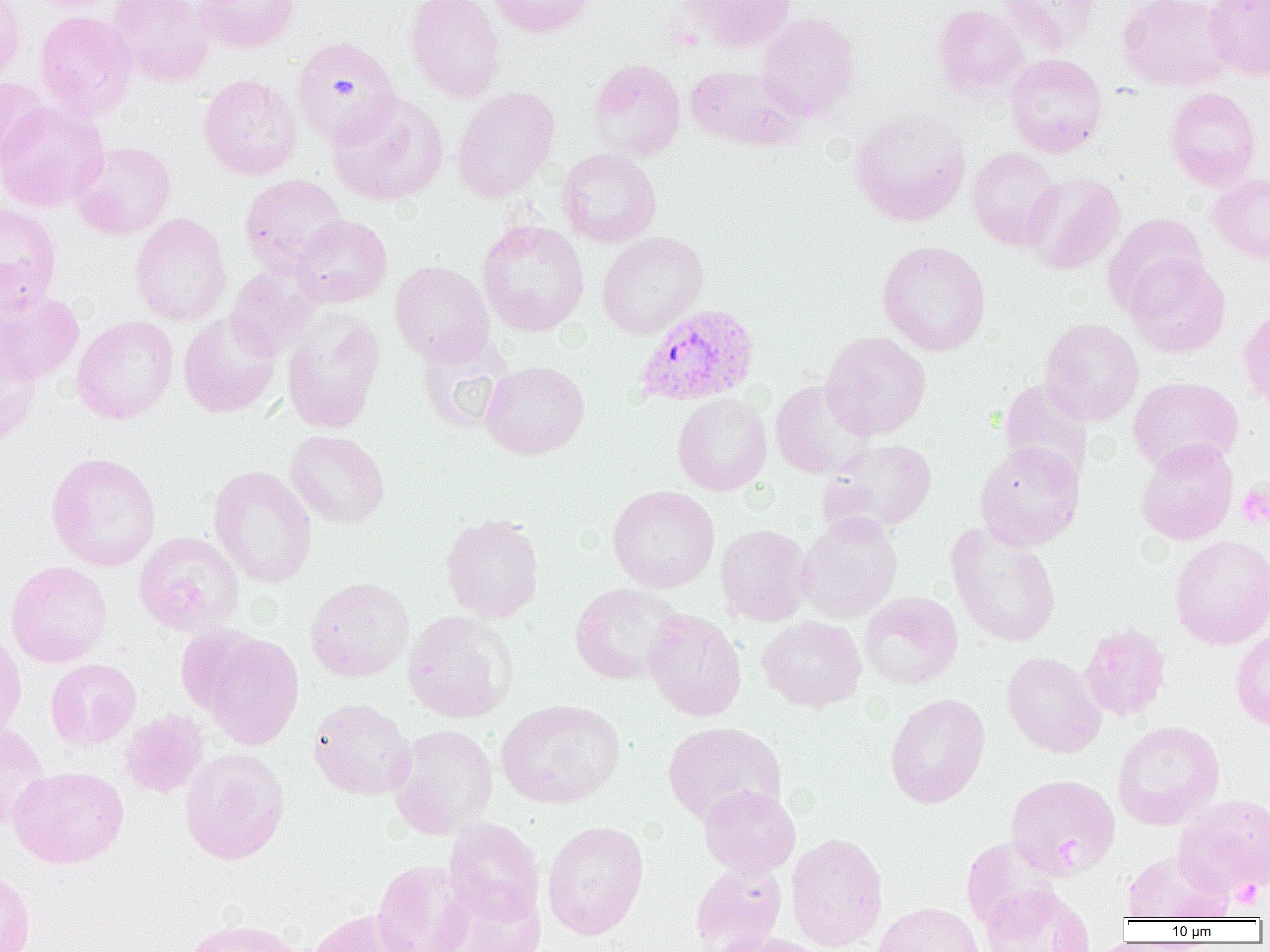

slide-level diagnosis = Plasmodium vivax
preparation = thin blood film
magnification = 1000x
platelet locations = approximate bounding boxes as [x1, y1, x2, y2] in pixels: [1236, 483, 1270, 529], [1054, 836, 1080, 871], [1230, 880, 1264, 910]
image size = 1270×952 pixels
Plasmodium vivax-infected red blood cell locations = approximate bounding boxes as [x1, y1, x2, y2] in pixels: [635, 307, 763, 412]
uninfected red blood cell locations = approximate bounding boxes as [x1, y1, x2, y2] in pixels: [0, 0, 28, 82], [107, 0, 215, 87], [193, 0, 300, 53], [404, 0, 505, 102], [487, 0, 594, 37], [681, 0, 798, 51], [998, 0, 1100, 56], [1116, 0, 1235, 92], [1203, 0, 1270, 81], [932, 4, 1029, 101], [34, 11, 137, 119], [756, 11, 860, 122], [291, 36, 401, 147], [1004, 53, 1108, 157], [587, 58, 686, 162], [685, 64, 804, 151], [198, 74, 302, 181], [0, 77, 48, 167], [452, 87, 560, 203], [1165, 87, 1262, 190], [328, 92, 448, 207], [0, 99, 109, 212], [848, 109, 970, 226], [70, 140, 176, 241], [556, 147, 662, 248], [967, 147, 1063, 251], [1208, 172, 1270, 264], [1022, 173, 1125, 275], [240, 174, 348, 277], [0, 203, 62, 312], [130, 212, 232, 327], [1102, 213, 1209, 316], [291, 215, 393, 307], [477, 219, 589, 336], [597, 232, 709, 339], [877, 240, 991, 357], [1125, 253, 1231, 357], [390, 260, 495, 366], [225, 267, 317, 361], [0, 287, 84, 386], [1238, 305, 1270, 417], [282, 310, 385, 433], [178, 312, 281, 418], [72, 315, 179, 424], [1039, 318, 1144, 425], [820, 331, 931, 440], [416, 333, 514, 434], [0, 343, 42, 447], [480, 360, 590, 460], [1128, 376, 1243, 472], [998, 378, 1094, 486], [770, 379, 876, 479], [672, 392, 772, 496], [284, 430, 390, 528], [818, 438, 937, 537], [1135, 438, 1238, 546], [975, 442, 1085, 550], [45, 451, 162, 572], [209, 465, 318, 588], [607, 485, 720, 593], [797, 512, 903, 623], [441, 514, 544, 623], [945, 523, 1062, 647], [715, 524, 813, 626], [133, 531, 245, 636], [1169, 535, 1270, 650], [5, 560, 112, 668], [305, 576, 414, 682], [569, 583, 685, 685], [859, 591, 963, 689], [642, 608, 747, 722], [402, 609, 518, 723], [757, 616, 867, 712], [1079, 623, 1171, 722], [1230, 624, 1270, 732], [0, 630, 27, 741], [199, 631, 304, 749], [1002, 651, 1106, 758], [45, 658, 141, 750], [884, 693, 990, 808], [308, 697, 415, 800], [496, 698, 626, 809], [119, 709, 209, 799], [1112, 720, 1224, 830], [662, 721, 786, 827], [0, 722, 50, 833], [388, 724, 499, 838], [179, 747, 290, 865], [7, 765, 129, 869], [1005, 774, 1120, 880], [698, 785, 801, 878], [1172, 794, 1270, 898], [443, 818, 545, 924], [542, 820, 649, 940], [786, 832, 888, 951], [960, 837, 1062, 935], [1122, 850, 1232, 922], [372, 859, 474, 952], [690, 862, 787, 952], [0, 866, 35, 952], [433, 883, 546, 952], [981, 886, 1095, 952], [873, 902, 985, 952], [307, 908, 416, 952], [178, 917, 309, 952], [709, 931, 823, 952]
field of view = single
modality = optical microscopy